Name the parasite shown.
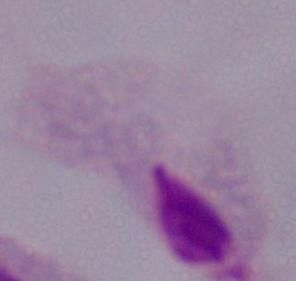

A trichomonad.

modality = photomicrograph
magnification = 1000x